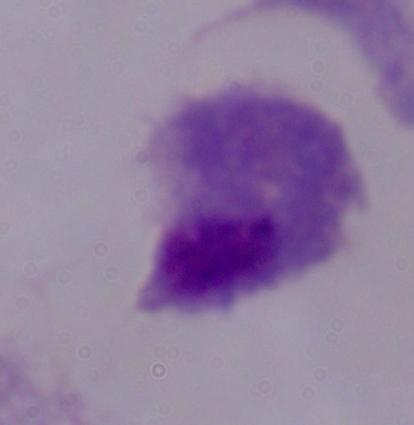

Summary:
  - Identification: trichomonad
  - Magnification: 1000x
  - Modality: micrograph